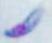
Captured at 1000x magnification. Micrograph. Toxoplasma gondii is shown.